Report the malaria status of this cell.
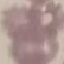

Uninfected.

stain = Giemsa
preparation = thin smear
image type = automatically extracted cell patch, resized to 64 × 64 pixels
capture = smartphone through the microscope eyepiece